Outline platelets.
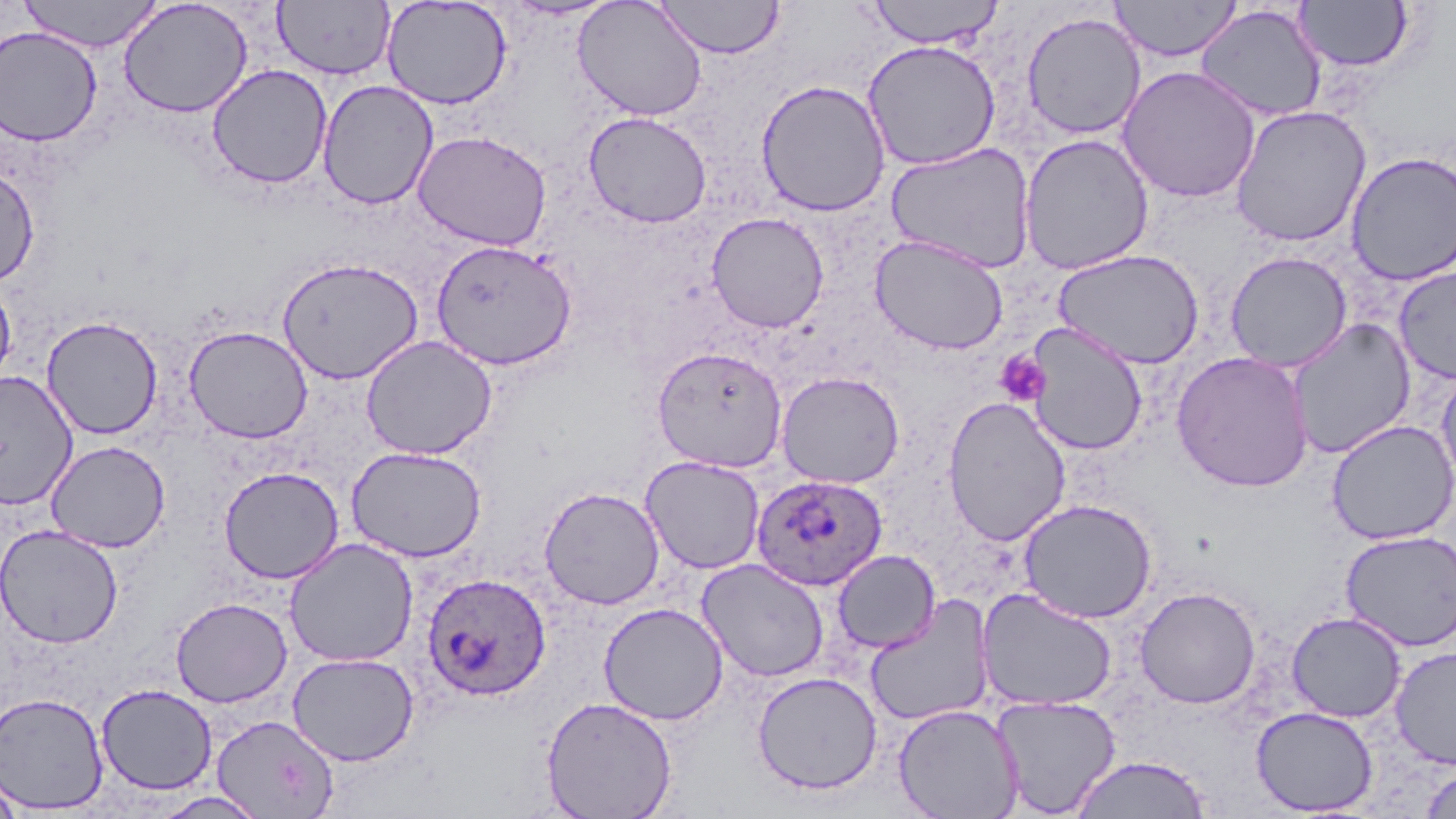
Approximate bounding boxes as (x1, y1, x2, y2) in pixels.
Platelets: (994, 349, 1050, 407).

Summary:
  - Plasmodium ovale-infected red blood cell locations: (752, 473, 888, 591), (422, 573, 551, 702)
  - Uninfected red blood cell locations: (18, 0, 163, 53), (118, 0, 253, 118), (382, 0, 512, 109), (573, 0, 708, 121), (864, 0, 1006, 49), (1110, 0, 1242, 61), (273, 1, 395, 80), (655, 1, 785, 59), (1294, 1, 1414, 73), (1195, 4, 1327, 123), (1021, 11, 1146, 140), (1, 26, 103, 146), (861, 39, 1002, 170), (207, 64, 332, 189), (1117, 65, 1261, 203), (317, 79, 439, 210), (755, 79, 891, 217), (1230, 104, 1371, 247), (584, 112, 712, 228), (413, 130, 552, 250), (1019, 133, 1155, 274), (885, 142, 1036, 274), (1345, 151, 1456, 286), (0, 165, 39, 287), (706, 212, 829, 332), (870, 235, 1008, 355), (430, 239, 577, 370), (1053, 248, 1205, 369), (1225, 251, 1352, 372), (276, 256, 424, 384), (1393, 266, 1456, 384), (0, 275, 17, 394), (41, 315, 164, 439), (1286, 318, 1416, 459), (1024, 323, 1148, 456), (184, 325, 313, 444), (360, 335, 497, 460), (652, 346, 788, 472), (1171, 351, 1314, 492), (1435, 364, 1456, 494), (0, 371, 78, 509), (776, 371, 905, 489), (942, 396, 1071, 546), (1326, 419, 1456, 545), (45, 440, 171, 553), (345, 445, 487, 562), (640, 455, 765, 574), (219, 466, 344, 583), (538, 486, 666, 610), (1018, 498, 1158, 623), (0, 524, 123, 648), (1339, 530, 1456, 651), (284, 538, 419, 667), (832, 549, 941, 653), (696, 559, 830, 682), (976, 587, 1118, 711), (1134, 587, 1261, 708), (864, 595, 996, 727), (170, 597, 293, 707), (599, 603, 728, 725), (1286, 612, 1406, 722), (1390, 646, 1456, 769), (287, 652, 419, 766), (751, 671, 883, 795), (96, 684, 218, 795), (0, 692, 110, 814), (991, 695, 1122, 817), (541, 696, 678, 819), (892, 703, 1025, 819), (1251, 706, 1379, 815), (211, 714, 340, 818), (1070, 755, 1211, 818), (1420, 765, 1456, 818), (0, 770, 24, 819), (150, 791, 270, 819)
  - Slide-level diagnosis: Plasmodium ovale
  - Image size: 1456×819 pixels
  - Magnification: 1000x
  - Field of view: single
  - Stain: May-Grünwald-Giemsa
  - Preparation: thin blood smear
  - Modality: optical microscopy